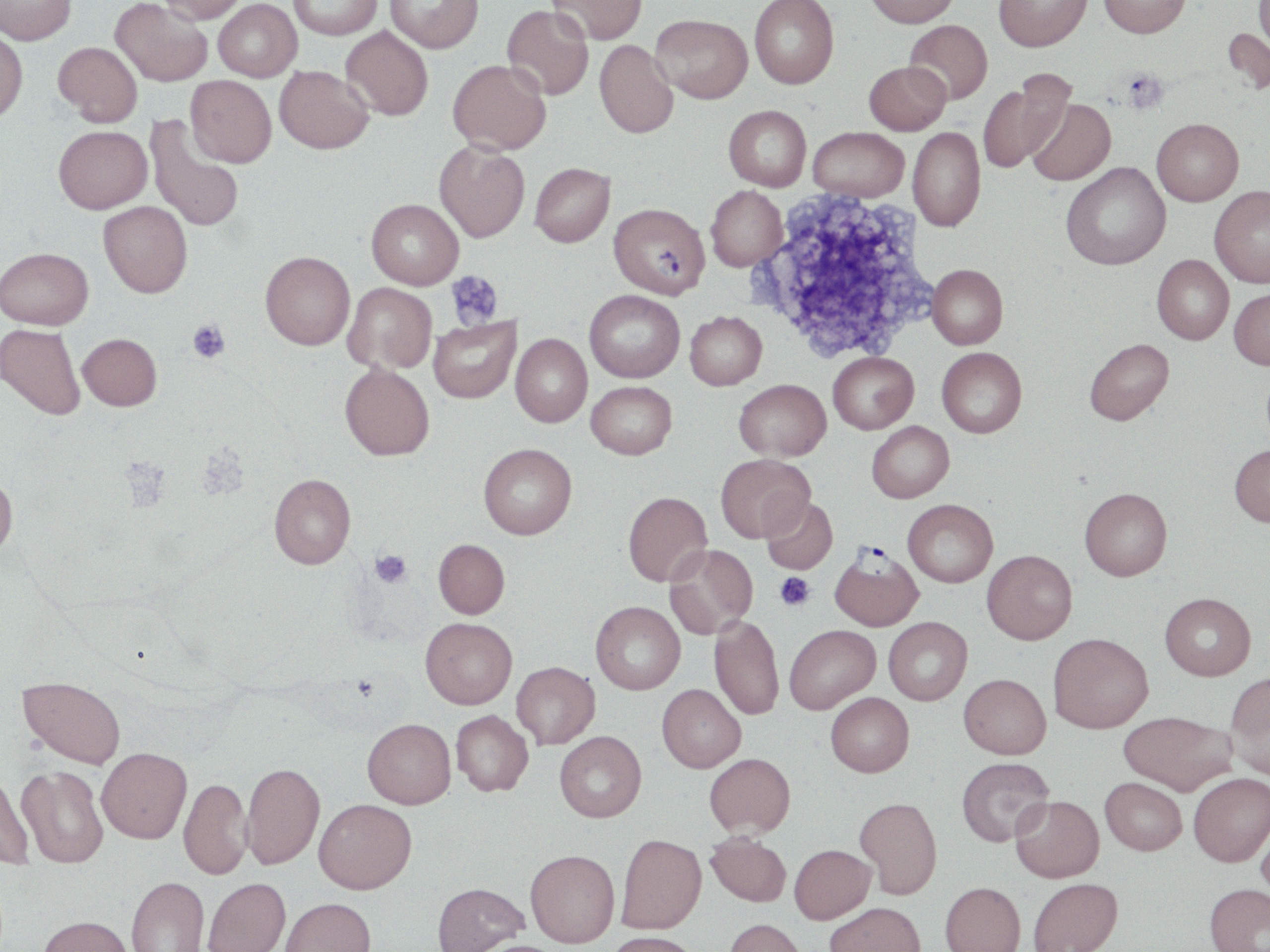

Summary:
  - Coordinate format: approximate bounding boxes as named x1/y1/x2/y2 corners in pixels
  - Plasmodium falciparum-infected red blood cell locations: (x1=609, y1=202, x2=710, y2=298), (x1=829, y1=546, x2=923, y2=631)
  - Platelet locations: (x1=1121, y1=67, x2=1169, y2=114), (x1=747, y1=187, x2=941, y2=365), (x1=446, y1=270, x2=504, y2=330), (x1=188, y1=319, x2=229, y2=363), (x1=119, y1=457, x2=169, y2=509), (x1=370, y1=549, x2=412, y2=587), (x1=775, y1=572, x2=815, y2=611), (x1=353, y1=676, x2=378, y2=699)
  - Uninfected red blood cell locations: (x1=0, y1=0, x2=76, y2=45), (x1=111, y1=0, x2=212, y2=86), (x1=158, y1=0, x2=246, y2=24), (x1=213, y1=0, x2=301, y2=81), (x1=289, y1=0, x2=383, y2=39), (x1=386, y1=0, x2=484, y2=53), (x1=548, y1=0, x2=647, y2=44), (x1=749, y1=0, x2=839, y2=89), (x1=865, y1=0, x2=959, y2=28), (x1=994, y1=0, x2=1091, y2=51), (x1=1099, y1=0, x2=1191, y2=37), (x1=1251, y1=0, x2=1270, y2=61), (x1=502, y1=5, x2=594, y2=100), (x1=651, y1=14, x2=753, y2=103), (x1=904, y1=19, x2=992, y2=105), (x1=341, y1=26, x2=433, y2=120), (x1=0, y1=27, x2=27, y2=123), (x1=1222, y1=27, x2=1270, y2=97), (x1=594, y1=40, x2=678, y2=138), (x1=53, y1=41, x2=142, y2=127), (x1=448, y1=59, x2=551, y2=155), (x1=864, y1=61, x2=951, y2=135), (x1=274, y1=65, x2=373, y2=154), (x1=977, y1=73, x2=1072, y2=174), (x1=185, y1=75, x2=277, y2=168), (x1=1027, y1=97, x2=1116, y2=186), (x1=724, y1=105, x2=811, y2=191), (x1=145, y1=116, x2=245, y2=233), (x1=1152, y1=118, x2=1243, y2=206), (x1=53, y1=125, x2=152, y2=213), (x1=809, y1=127, x2=909, y2=202), (x1=908, y1=128, x2=985, y2=231), (x1=434, y1=142, x2=530, y2=243), (x1=530, y1=162, x2=615, y2=247), (x1=1060, y1=162, x2=1170, y2=270), (x1=706, y1=185, x2=787, y2=271), (x1=1209, y1=186, x2=1270, y2=287), (x1=367, y1=199, x2=464, y2=289), (x1=99, y1=201, x2=192, y2=297), (x1=0, y1=247, x2=93, y2=329), (x1=260, y1=251, x2=355, y2=350), (x1=1152, y1=255, x2=1234, y2=344), (x1=927, y1=264, x2=1008, y2=349), (x1=343, y1=282, x2=437, y2=373), (x1=1229, y1=286, x2=1270, y2=369), (x1=584, y1=290, x2=685, y2=382), (x1=685, y1=311, x2=767, y2=390), (x1=429, y1=317, x2=521, y2=403), (x1=0, y1=323, x2=86, y2=419), (x1=78, y1=333, x2=162, y2=410), (x1=511, y1=334, x2=592, y2=427), (x1=1084, y1=338, x2=1174, y2=425), (x1=936, y1=346, x2=1027, y2=437), (x1=828, y1=351, x2=919, y2=433), (x1=340, y1=363, x2=434, y2=460), (x1=735, y1=379, x2=831, y2=460), (x1=586, y1=381, x2=677, y2=459), (x1=867, y1=421, x2=954, y2=502), (x1=479, y1=443, x2=577, y2=539), (x1=1229, y1=443, x2=1270, y2=527), (x1=716, y1=454, x2=814, y2=542), (x1=0, y1=470, x2=18, y2=561), (x1=269, y1=474, x2=356, y2=569), (x1=1079, y1=487, x2=1172, y2=580), (x1=623, y1=491, x2=712, y2=586), (x1=761, y1=497, x2=838, y2=575), (x1=902, y1=499, x2=998, y2=587), (x1=434, y1=539, x2=509, y2=618), (x1=665, y1=544, x2=756, y2=636), (x1=982, y1=549, x2=1077, y2=644), (x1=1159, y1=592, x2=1256, y2=680), (x1=591, y1=601, x2=685, y2=694), (x1=710, y1=614, x2=784, y2=720), (x1=420, y1=617, x2=517, y2=709), (x1=883, y1=617, x2=972, y2=705), (x1=784, y1=625, x2=880, y2=713), (x1=1048, y1=633, x2=1153, y2=733), (x1=512, y1=662, x2=600, y2=748), (x1=1225, y1=671, x2=1270, y2=779), (x1=959, y1=673, x2=1051, y2=758), (x1=18, y1=676, x2=126, y2=769), (x1=657, y1=683, x2=746, y2=772), (x1=825, y1=692, x2=914, y2=777), (x1=451, y1=710, x2=534, y2=796), (x1=1118, y1=710, x2=1237, y2=795), (x1=362, y1=718, x2=456, y2=809), (x1=555, y1=731, x2=646, y2=822), (x1=97, y1=747, x2=192, y2=843), (x1=704, y1=753, x2=796, y2=836), (x1=956, y1=756, x2=1054, y2=846), (x1=241, y1=761, x2=326, y2=870), (x1=17, y1=765, x2=109, y2=868), (x1=0, y1=770, x2=35, y2=869), (x1=1188, y1=772, x2=1270, y2=866), (x1=1100, y1=777, x2=1187, y2=855), (x1=179, y1=778, x2=251, y2=880), (x1=1010, y1=795, x2=1104, y2=882), (x1=855, y1=796, x2=942, y2=899), (x1=314, y1=798, x2=417, y2=893), (x1=1256, y1=817, x2=1270, y2=907), (x1=706, y1=832, x2=791, y2=906), (x1=616, y1=833, x2=706, y2=934), (x1=789, y1=844, x2=876, y2=923), (x1=525, y1=849, x2=620, y2=947), (x1=126, y1=876, x2=209, y2=952), (x1=203, y1=877, x2=290, y2=952), (x1=1028, y1=877, x2=1123, y2=952), (x1=940, y1=881, x2=1025, y2=952), (x1=432, y1=882, x2=528, y2=952), (x1=1204, y1=883, x2=1270, y2=952), (x1=281, y1=897, x2=375, y2=952), (x1=824, y1=901, x2=925, y2=952), (x1=38, y1=915, x2=134, y2=952), (x1=724, y1=918, x2=806, y2=952), (x1=606, y1=932, x2=700, y2=952), (x1=473, y1=939, x2=566, y2=952)
  - Slide-level diagnosis: Plasmodium falciparum
  - Image size: 1270×952 pixels
  - Magnification: 1000x
  - Field of view: one of a larger specimen
  - Modality: optical microscopy
  - Preparation: thin blood film
  - Stain: May-Grünwald-Giemsa